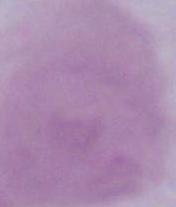
Summary:
  - Magnification: 1000x
  - Modality: photomicrograph
  - Identification: red blood cell